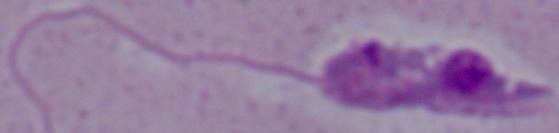

Summary:
  - Modality: photomicrograph
  - Identification: Leishmania
  - Magnification: 1000x